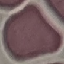
Summary:
  - Result: negative for malaria parasites
  - Image type: automatically extracted cell patch, resized to 64 × 64 pixels
  - Capture: smartphone through the microscope eyepiece
  - Stain: Giemsa
  - Preparation: thin blood film